Name the blood parasite species.
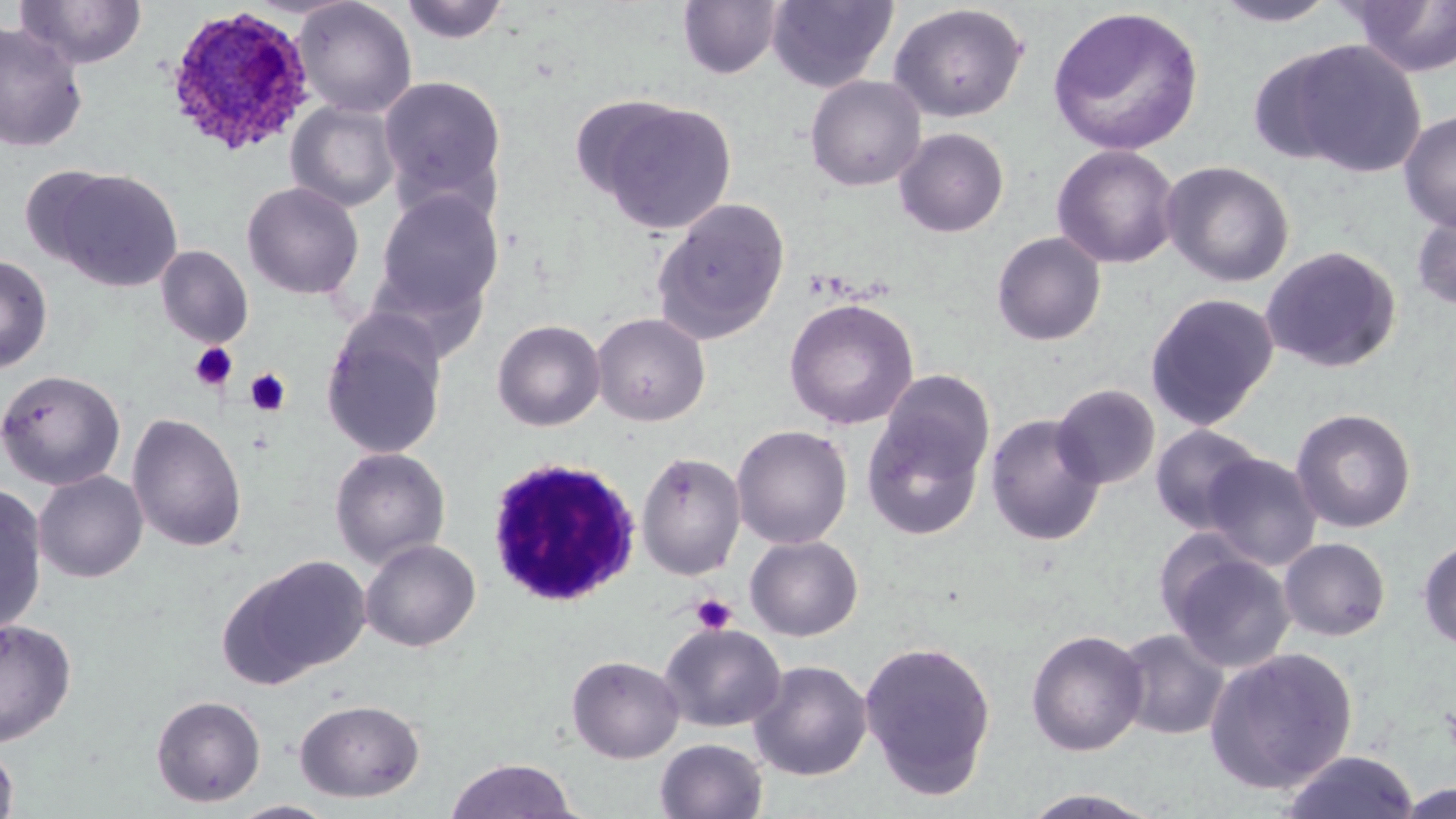
Plasmodium ovale.

field of view = one of a larger specimen
stain = May-Grünwald-Giemsa
modality = light microscopy
preparation = thin blood film
white blood cell locations = approximate bounding boxes as [x1, y1, x2, y2] in pixels: [486, 456, 642, 607]
magnification = 1000x
platelet locations = approximate bounding boxes as [x1, y1, x2, y2] in pixels: [189, 342, 238, 391], [245, 368, 291, 416], [690, 593, 737, 634]
image size = 1456×819 pixels
uninfected red blood cell locations = approximate bounding boxes as [x1, y1, x2, y2] in pixels: [16, 0, 147, 69], [291, 0, 417, 118], [399, 0, 511, 45], [766, 0, 899, 92], [677, 1, 784, 80], [1211, 1, 1342, 28], [1346, 1, 1456, 77], [888, 3, 1028, 123], [1047, 6, 1205, 156], [0, 21, 88, 153], [1273, 39, 1427, 178], [378, 74, 509, 216], [806, 75, 926, 192], [593, 99, 738, 235], [286, 100, 402, 213], [1398, 109, 1456, 232], [894, 128, 1009, 237], [1051, 144, 1181, 270], [1161, 160, 1295, 288], [49, 168, 183, 291], [242, 182, 364, 300], [372, 189, 504, 320], [652, 197, 791, 344], [1410, 207, 1456, 311], [992, 232, 1106, 345], [155, 245, 253, 348], [1260, 245, 1402, 373], [0, 254, 53, 374], [1145, 292, 1280, 431], [784, 298, 919, 430], [591, 312, 711, 426], [320, 313, 449, 460], [492, 319, 606, 432], [0, 369, 126, 490], [1051, 383, 1160, 490], [860, 398, 989, 542], [1290, 408, 1417, 533], [126, 412, 247, 553], [985, 413, 1106, 546], [1150, 423, 1265, 534], [732, 425, 853, 549], [329, 447, 451, 569], [636, 451, 747, 580], [1202, 452, 1322, 570], [33, 470, 148, 583], [0, 482, 48, 636], [745, 535, 863, 641], [1278, 537, 1391, 641], [1417, 537, 1456, 652], [359, 538, 481, 652], [1161, 541, 1297, 673], [224, 554, 371, 684], [0, 618, 77, 747], [658, 622, 786, 733], [1114, 628, 1229, 740], [1026, 629, 1148, 757], [859, 639, 997, 798], [1204, 647, 1359, 794], [566, 654, 685, 763], [748, 660, 872, 781], [151, 694, 266, 807], [294, 698, 425, 802], [655, 738, 768, 819], [0, 739, 19, 819], [1276, 749, 1420, 819], [444, 758, 581, 818], [1015, 788, 1168, 818], [228, 800, 339, 819]
Plasmodium ovale-infected red blood cell locations = approximate bounding boxes as [x1, y1, x2, y2] in pixels: [161, 8, 314, 158]